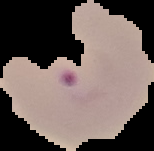
From a thin blood smear. The area outside the segmented cell region is set to black. Image is 154×151 pixels. Malaria status: parasitized.